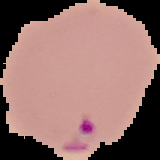

result = malaria parasites detected
image type = segmented cell region with the area outside set to black
image size = 160×160 pixels
preparation = thin blood smear